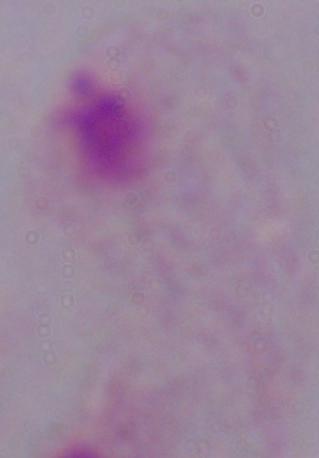

Summary:
  - Magnification: 1000x
  - Modality: photomicrograph
  - Identification: trichomonad